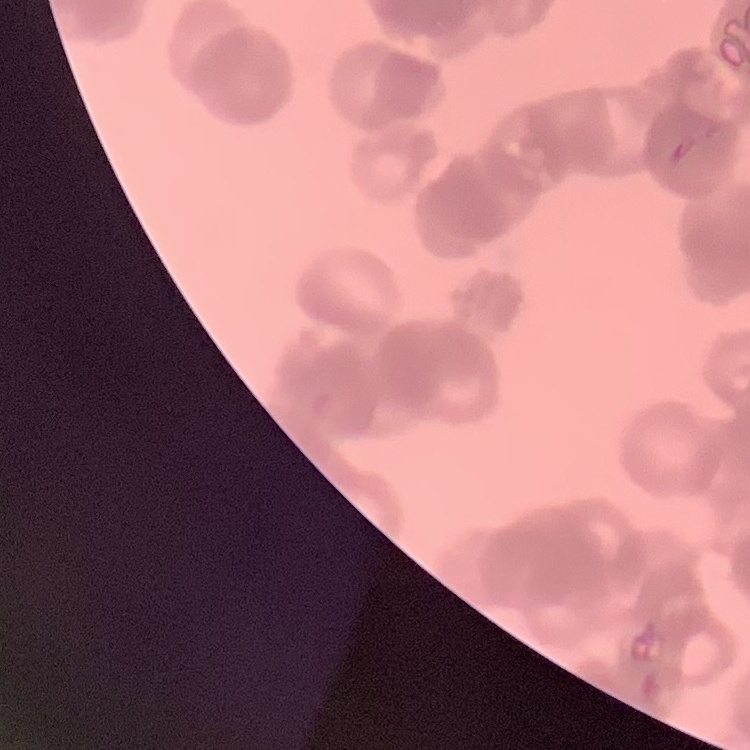
Summary:
  - Red blood cell morphology: rouleaux formation
  - Stain: Field's or Giemsa
  - Preparation: thin peripheral smear
  - Image type: one tile cut from a larger photomicrograph